Identify the parasite.
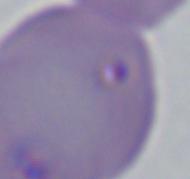
Babesia.

{
  "modality": "micrograph",
  "magnification": "1000x"
}